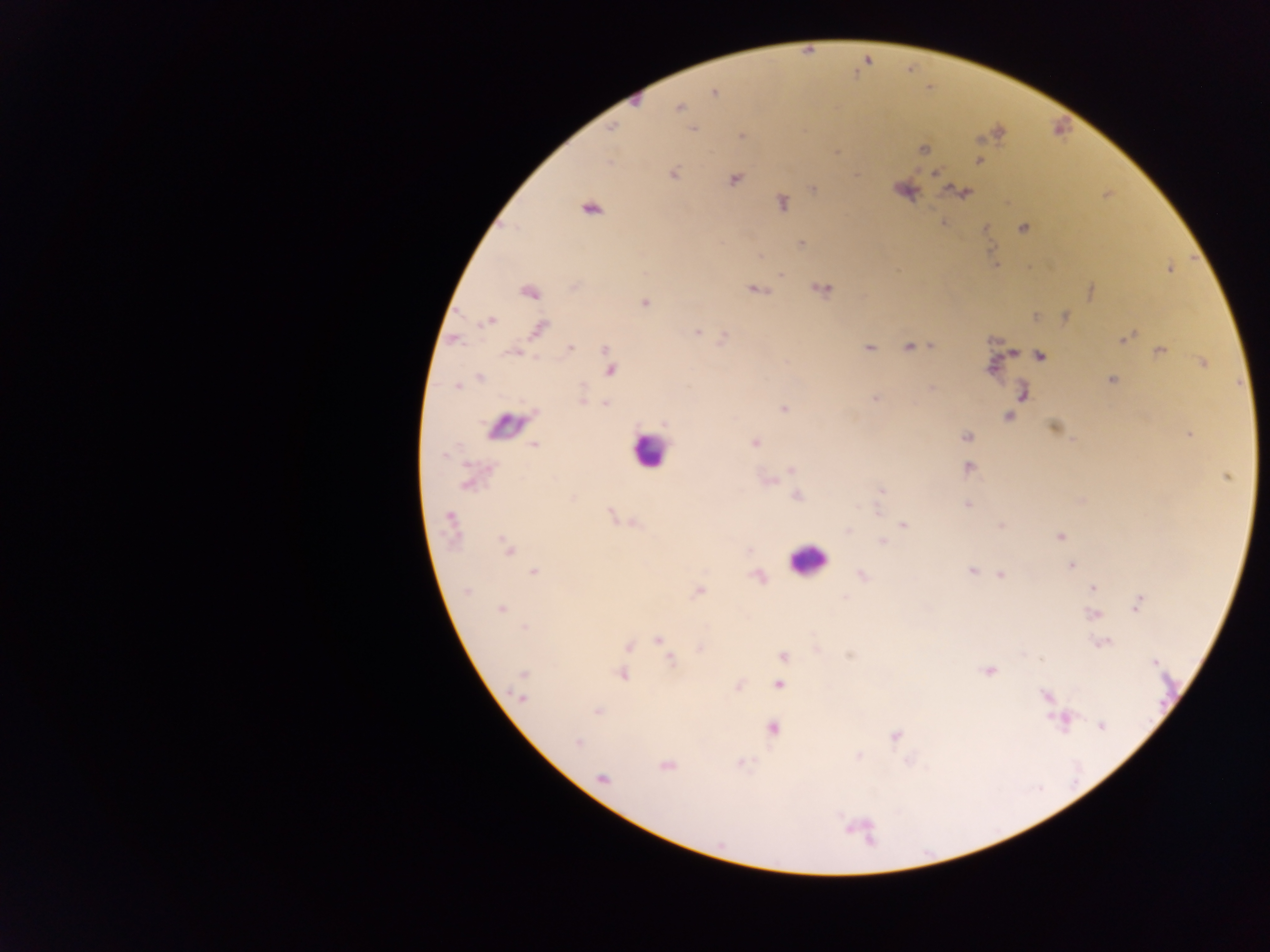

image size = 1270×952 pixels
leukocyte locations = approximate centers as x y in pixels: 507 426; 648 451; 807 561
Plasmodium parasite locations = approximate centers as x y in pixels: 714 92; 634 98; 678 107; 611 127; 693 129; 740 136; 922 148; 836 153; 980 161; 935 173; 673 174; 734 179; 813 189; 903 189; 962 192; 781 202; 589 208; 1023 227; 985 228; 801 244; 996 265; 1169 267; 780 273; 821 288; 755 290; 1091 290; 529 291; 645 303; 1034 316; 1064 317; 488 321; 538 328; 696 330; 725 337; 1124 337; 907 347; 932 347; 570 348; 868 348; 606 350; 1159 351; 514 352; 1039 355; 1201 362; 609 368; 479 377; 1112 379; 457 386; 930 388; 1022 392; 581 398; 875 398; 605 403; 783 408; 1009 416; 663 422; 1054 428; 1188 433; 966 437; 755 442; 534 445; 967 468; 792 469; 1226 477; 766 480; 469 481; 881 490; 797 495; 1080 500; 967 503; 612 516; 450 522; 631 522; 903 525; 1002 526; 848 530; 1059 536; 883 542; 507 548; 1071 565; 971 571; 534 572; 862 574; 999 574; 757 576; 1093 588; 697 591; 465 592; 845 598; 1136 603; 501 608; 1094 614; 525 628; 658 639; 1102 642; 634 643; 628 646; 699 648; 783 656; 670 660; 1153 661; 624 663; 988 670; 620 673; 523 675; 778 684; 738 686; 1045 696; 521 697; 597 710; 1063 719; 1100 725; 771 727; 895 735; 577 743; 858 755; 741 763; 665 766; 602 779
country = Ghana
capture = mobile-phone photograph through a microscope
preparation = thick blood film
field of view = single